Give the extent of all Plasmodium vivax-infected red blood cells.
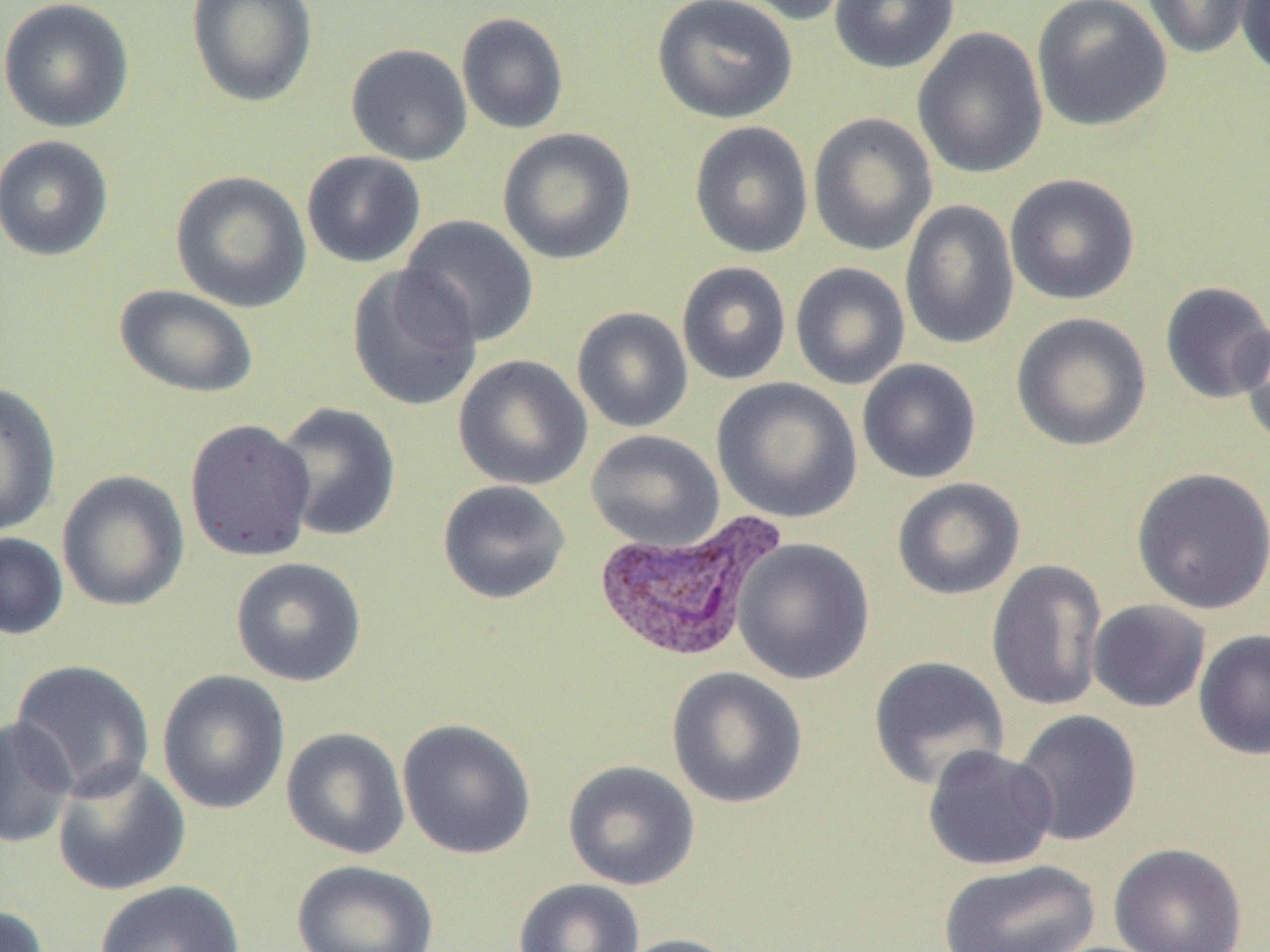

Approximate bounding boxes as named x1/y1/x2/y2 corners in pixels.
Plasmodium vivax-infected red blood cells: (x1=590, y1=508, x2=787, y2=664).

slide-level diagnosis = Plasmodium vivax
image size = 1270×952 pixels
field of view = single
preparation = thin blood film
uninfected red blood cell locations = approximate bounding boxes as named x1/y1/x2/y2 corners in pixels: (x1=0, y1=0, x2=136, y2=133), (x1=186, y1=0, x2=318, y2=107), (x1=652, y1=0, x2=799, y2=124), (x1=718, y1=0, x2=854, y2=26), (x1=829, y1=0, x2=959, y2=74), (x1=1031, y1=0, x2=1173, y2=132), (x1=1140, y1=0, x2=1255, y2=60), (x1=1236, y1=0, x2=1270, y2=79), (x1=456, y1=12, x2=570, y2=135), (x1=912, y1=27, x2=1048, y2=179), (x1=345, y1=43, x2=473, y2=166), (x1=808, y1=112, x2=938, y2=256), (x1=689, y1=121, x2=813, y2=259), (x1=497, y1=127, x2=637, y2=265), (x1=0, y1=134, x2=115, y2=262), (x1=301, y1=150, x2=426, y2=269), (x1=170, y1=170, x2=313, y2=313), (x1=1004, y1=173, x2=1141, y2=306), (x1=899, y1=199, x2=1020, y2=350), (x1=399, y1=214, x2=540, y2=348), (x1=676, y1=261, x2=792, y2=385), (x1=790, y1=262, x2=910, y2=390), (x1=346, y1=265, x2=483, y2=412), (x1=1159, y1=281, x2=1270, y2=405), (x1=113, y1=284, x2=260, y2=399), (x1=571, y1=306, x2=693, y2=433), (x1=1010, y1=312, x2=1152, y2=452), (x1=1235, y1=317, x2=1270, y2=452), (x1=453, y1=354, x2=593, y2=491), (x1=857, y1=359, x2=982, y2=484), (x1=711, y1=377, x2=862, y2=523), (x1=0, y1=381, x2=62, y2=538), (x1=272, y1=402, x2=402, y2=543), (x1=184, y1=418, x2=317, y2=562), (x1=585, y1=430, x2=724, y2=551), (x1=1130, y1=466, x2=1270, y2=615), (x1=56, y1=470, x2=191, y2=612), (x1=892, y1=477, x2=1025, y2=601), (x1=437, y1=480, x2=571, y2=605), (x1=0, y1=531, x2=69, y2=640), (x1=733, y1=538, x2=875, y2=685), (x1=230, y1=556, x2=367, y2=687), (x1=986, y1=559, x2=1108, y2=712), (x1=1087, y1=599, x2=1211, y2=713), (x1=1193, y1=628, x2=1270, y2=760), (x1=868, y1=656, x2=1010, y2=790), (x1=10, y1=658, x2=156, y2=802), (x1=666, y1=667, x2=808, y2=809), (x1=157, y1=669, x2=291, y2=815), (x1=1011, y1=709, x2=1143, y2=847), (x1=0, y1=716, x2=77, y2=849), (x1=397, y1=717, x2=537, y2=860), (x1=281, y1=726, x2=410, y2=860), (x1=922, y1=745, x2=1059, y2=871), (x1=562, y1=760, x2=700, y2=891), (x1=51, y1=761, x2=191, y2=896), (x1=1109, y1=842, x2=1248, y2=952), (x1=290, y1=859, x2=440, y2=952), (x1=937, y1=859, x2=1101, y2=952), (x1=513, y1=878, x2=645, y2=952), (x1=94, y1=879, x2=246, y2=952), (x1=0, y1=904, x2=51, y2=952), (x1=613, y1=933, x2=743, y2=952)
modality = light microscopy
magnification = 1000x